Locate every uninfected red blood cell.
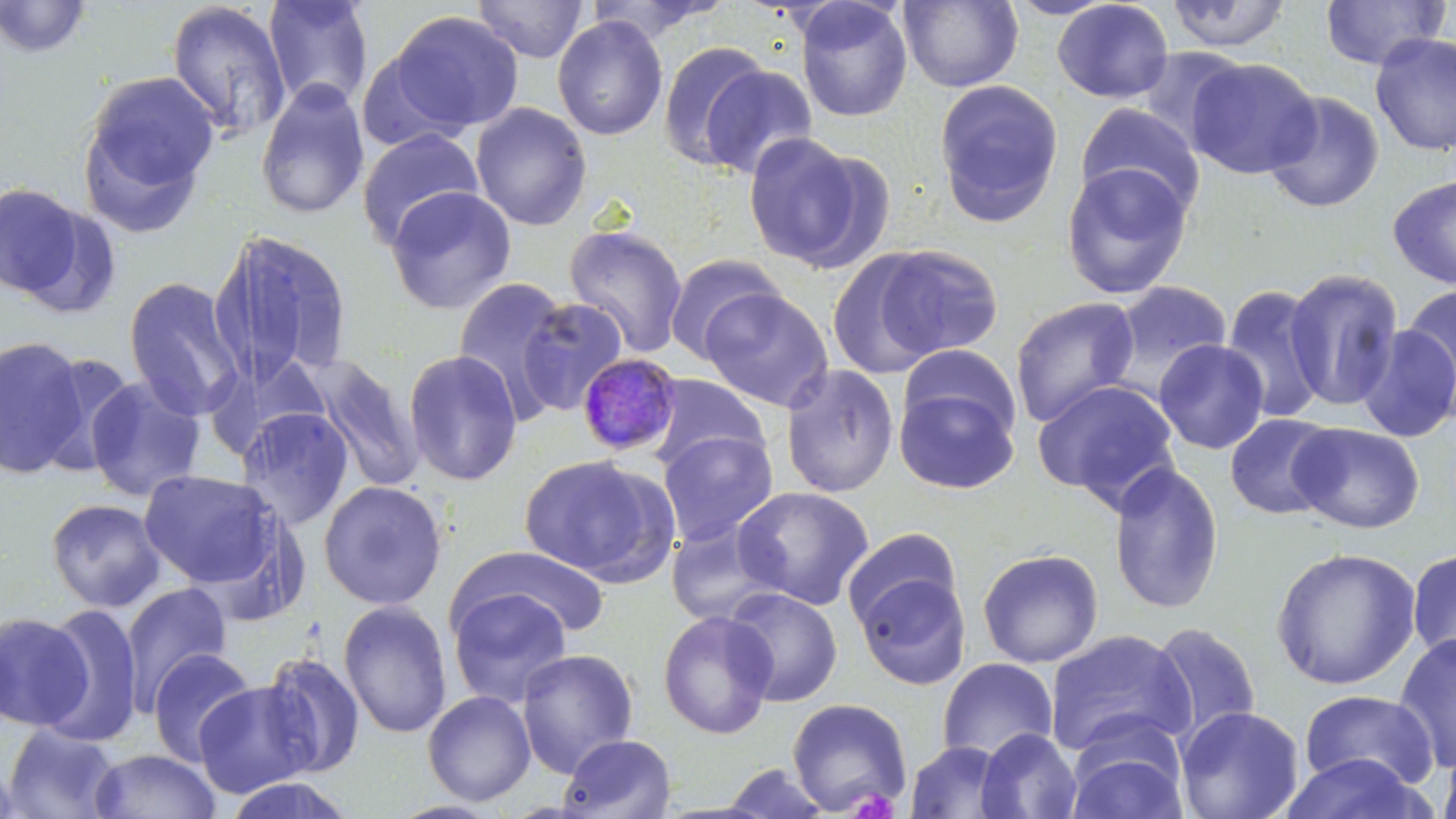
Approximate bounding boxes as (x1,y1)-(x2,y2) corner pairs in pixels.
Uninfected red blood cells: (1,0)-(93,59), (262,0)-(374,112), (472,0)-(589,62), (898,0)-(1023,92), (1003,0)-(1118,20), (1051,0)-(1174,103), (1165,0)-(1293,52), (1319,0)-(1450,70), (794,1)-(913,122), (165,2)-(292,143), (388,10)-(524,135), (552,15)-(669,141), (1369,32)-(1456,157), (658,41)-(773,171), (1135,47)-(1249,153), (1186,58)-(1321,179), (698,63)-(819,179), (80,71)-(218,225), (255,78)-(370,220), (933,79)-(1064,225), (1262,91)-(1385,213), (470,102)-(592,230), (1075,102)-(1205,219), (356,128)-(485,249), (741,131)-(873,271), (1060,163)-(1194,299), (1388,174)-(1456,290), (0,182)-(86,298), (385,186)-(517,315), (564,224)-(688,359), (211,228)-(354,387), (874,243)-(1004,360), (663,253)-(785,363), (824,253)-(946,378), (1283,268)-(1404,412), (451,275)-(574,422), (123,276)-(244,421), (1102,281)-(1233,401), (1221,283)-(1330,423), (1400,286)-(1456,408), (699,287)-(832,411), (515,296)-(630,416), (1009,296)-(1140,428), (1356,324)-(1456,443), (0,335)-(91,479), (1153,339)-(1270,455), (898,344)-(1022,442), (403,349)-(522,486), (35,350)-(137,476), (310,355)-(426,492), (780,363)-(899,499), (645,374)-(769,473), (85,375)-(206,502), (1033,378)-(1182,507), (894,387)-(1018,494), (235,406)-(355,530), (1224,413)-(1339,520), (1290,422)-(1425,534), (658,430)-(778,546), (517,454)-(668,581), (1108,462)-(1224,615), (138,469)-(282,589), (318,479)-(448,610), (733,485)-(875,610), (46,498)-(166,612), (665,519)-(783,626), (841,526)-(962,634), (452,545)-(613,641), (1271,547)-(1421,690), (977,548)-(1104,668), (1406,548)-(1456,668), (853,569)-(971,691), (119,583)-(232,713), (448,586)-(574,707), (724,586)-(843,707), (337,600)-(453,739), (38,603)-(144,747), (0,610)-(92,731), (657,610)-(778,740), (1148,622)-(1262,742), (1044,629)-(1195,758), (1393,634)-(1456,774), (147,647)-(256,766), (516,648)-(639,777), (261,653)-(366,778), (936,657)-(1058,763), (193,679)-(318,798), (422,690)-(536,806), (1299,690)-(1439,792), (787,697)-(913,816), (1175,706)-(1304,819), (2,724)-(122,818), (975,728)-(1082,819), (1066,729)-(1189,819), (556,733)-(677,819), (905,741)-(1014,819), (1439,741)-(1456,819), (88,748)-(222,819), (1278,752)-(1433,819), (0,760)-(28,817), (718,763)-(834,818), (219,776)-(360,819).

slide-level diagnosis = Plasmodium malariae
modality = optical microscopy
preparation = thin blood film
Plasmodium malariae-infected red blood cell locations = approximate bounding boxes as (x1,y1)-(x2,y2) corner pairs in pixels: (576,356)-(683,460)
image size = 1456×819 pixels
magnification = 1000x
stain = May-Grünwald-Giemsa
field of view = single
platelet locations = approximate bounding boxes as (x1,y1)-(x2,y2) corner pairs in pixels: (846,787)-(901,818)